Assess this cell for malaria.
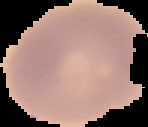
Uninfected.

preparation: thin blood smear
image_size: 148×127 pixels
image_type: cell region segmented out of the field of view; surrounding area masked to black